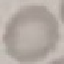
Result: no malaria parasites seen. Acquired by smartphone through the microscope eyepiece. Thin blood film. Giemsa stain. Cell patch, automatically extracted from a larger field of view and resized to 64 × 64 pixels.